Report the malaria status of this cell.
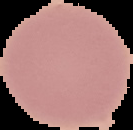

It is uninfected.

Summary:
  - Image size: 133×130 pixels
  - Image type: cell region segmented out of the field of view; surrounding area masked to black
  - Preparation: thin blood smear